Classify this cell by malaria status.
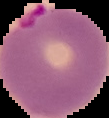

Parasitized.

From a thin blood smear. Cell region segmented out of the field of view; the surrounding area is masked to black. Image is 109×118 pixels.